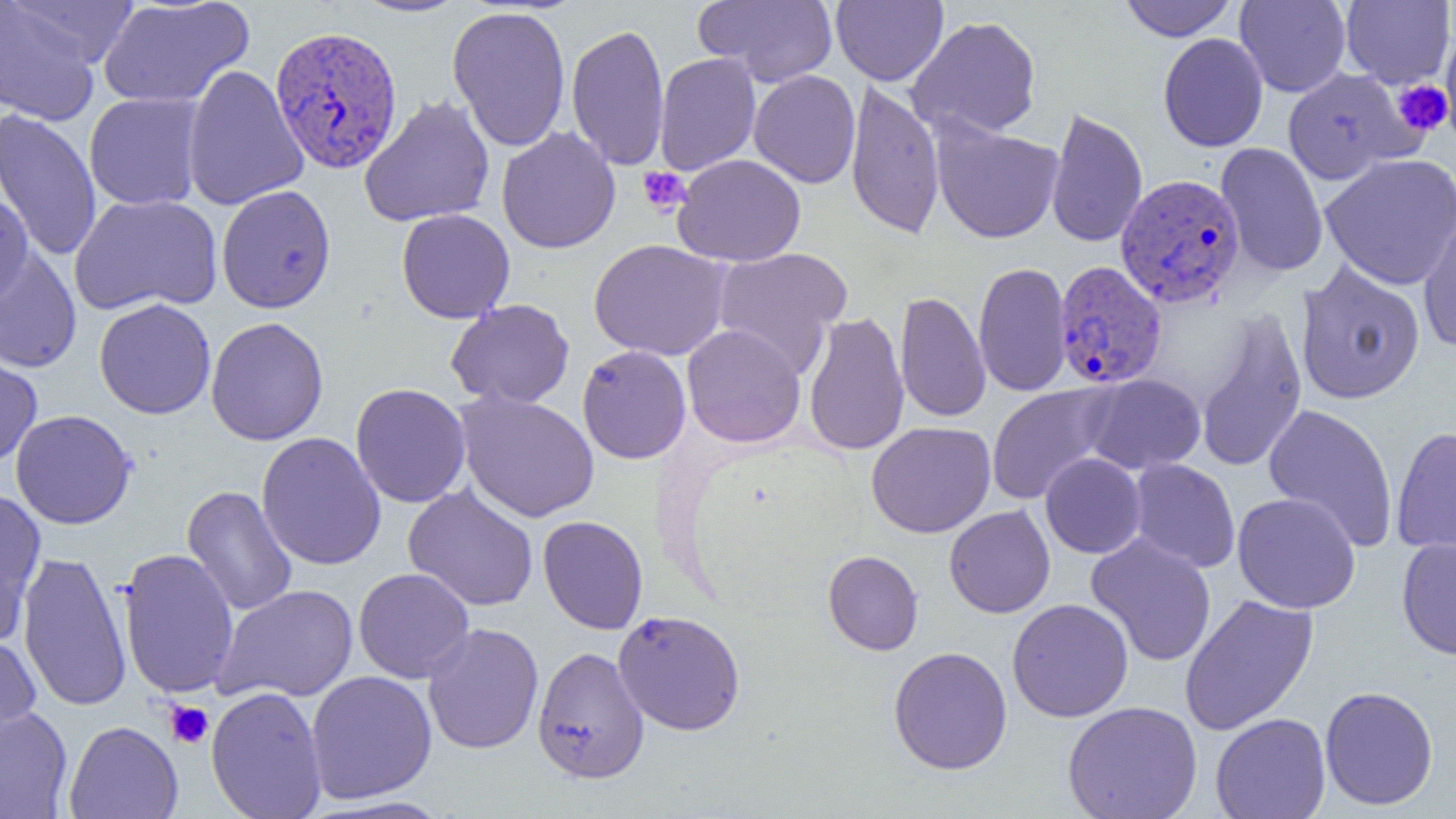
Summary:
  - Coordinate format: approximate bounding boxes as [x1, y1, x2, y2] in pixels
  - Platelet locations: [1393, 80, 1452, 136], [637, 166, 691, 216], [164, 700, 214, 749]
  - Uninfected red blood cell locations (subset): [6, 0, 141, 69], [97, 0, 254, 109], [350, 0, 470, 18], [693, 0, 838, 86], [832, 0, 948, 86], [1119, 0, 1237, 42], [1341, 0, 1455, 87], [1235, 1, 1352, 97], [0, 2, 105, 125], [447, 5, 571, 153], [906, 15, 1042, 140], [567, 23, 670, 172], [1440, 32, 1456, 141], [1158, 33, 1268, 152], [654, 52, 761, 176], [182, 64, 308, 211], [1281, 67, 1418, 185], [749, 70, 860, 188], [845, 80, 946, 240], [84, 92, 205, 211], [359, 94, 495, 227], [1045, 105, 1148, 249], [0, 108, 102, 262], [931, 119, 1064, 244], [496, 127, 621, 254], [1216, 142, 1329, 278], [1320, 153, 1456, 290], [672, 154, 807, 266], [216, 184, 337, 314], [69, 193, 223, 316], [1416, 206, 1456, 353], [396, 208, 515, 323], [588, 239, 731, 361], [0, 244, 82, 373], [711, 247, 852, 376], [1294, 260, 1426, 405], [973, 261, 1072, 398], [895, 290, 991, 423], [94, 298, 216, 419], [446, 298, 575, 409], [1195, 308, 1307, 474], [803, 311, 910, 457], [205, 317, 329, 446], [682, 324, 806, 448], [0, 345, 42, 468], [577, 345, 691, 464], [1083, 374, 1206, 474], [350, 383, 471, 508], [986, 384, 1118, 505], [456, 390, 599, 522], [1263, 403, 1399, 552], [11, 409, 137, 529], [866, 421, 996, 538], [1390, 425, 1456, 557], [257, 431, 386, 571], [1040, 453, 1146, 559], [1128, 458, 1241, 573], [182, 485, 298, 617], [402, 485, 539, 611], [0, 488, 47, 642], [1232, 492, 1361, 614], [944, 505, 1055, 618], [538, 515, 649, 634], [1085, 533, 1217, 666], [1396, 537, 1456, 660], [118, 548, 239, 699], [823, 550, 923, 655], [17, 551, 131, 712], [353, 567, 475, 683], [213, 584, 358, 703], [1179, 594, 1319, 736], [1007, 598, 1134, 722], [613, 609, 746, 735], [422, 622, 544, 755], [0, 634, 41, 749], [532, 646, 650, 784], [888, 646, 1013, 774], [306, 670, 437, 803], [206, 685, 327, 819], [1319, 685, 1439, 810], [1062, 700, 1202, 819], [0, 707, 73, 818], [1210, 712, 1331, 819], [64, 721, 183, 819]
  - Plasmodium vivax-infected red blood cell locations: [269, 24, 403, 174], [1115, 173, 1246, 307], [1053, 260, 1167, 389]
  - Slide-level diagnosis: Plasmodium vivax
  - Magnification: 1000x
  - Field of view: single
  - Preparation: thin blood film
  - Image size: 1456×819 pixels
  - Modality: light microscopy